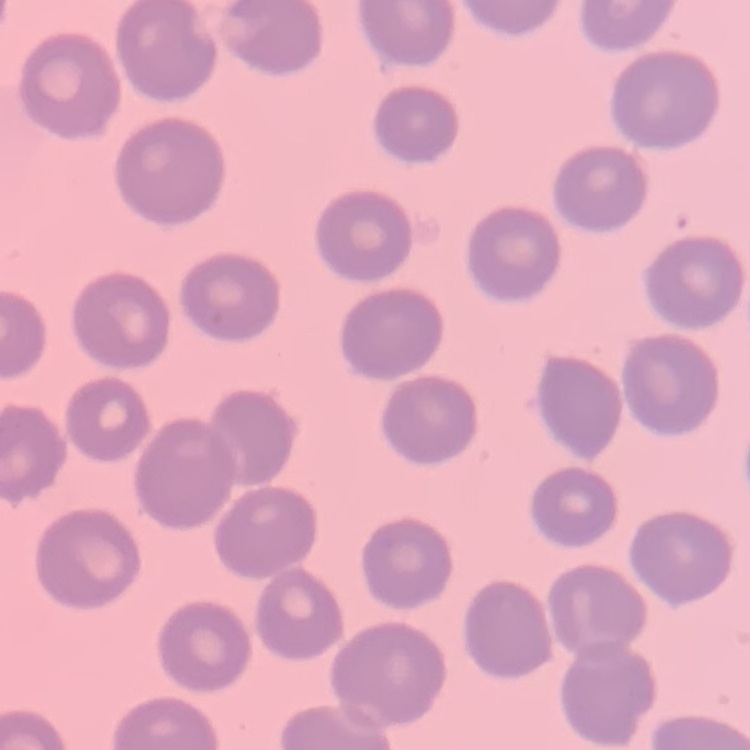
erythrocyte morphology = no rouleaux formation
preparation = thin blood smear
image type = one tile cut from a larger photomicrograph
stain = Field's or Giemsa